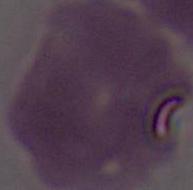

Summary:
  - Magnification: 1000x
  - Identification: erythrocyte
  - Modality: micrograph